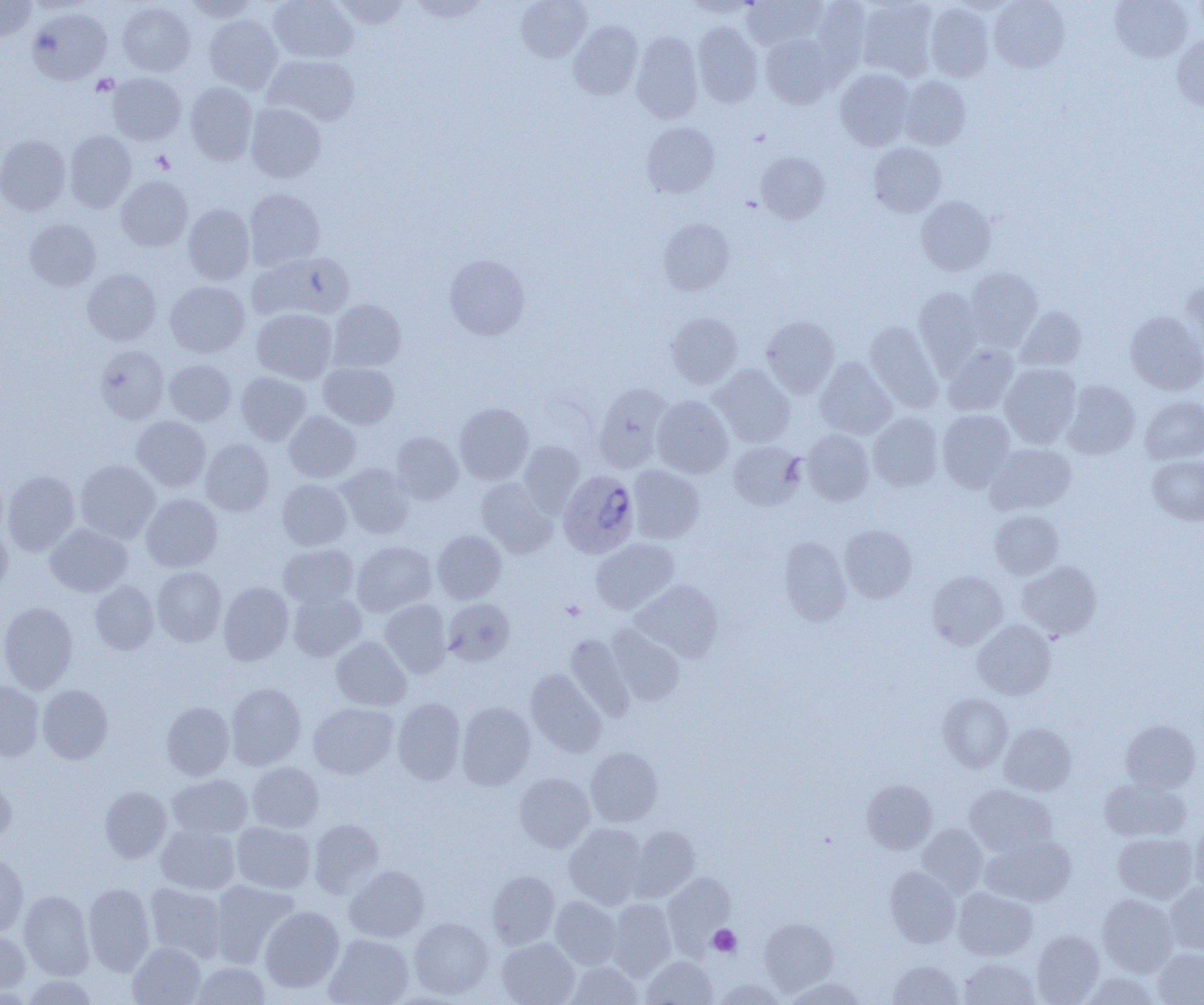
slide_level_diagnosis: Plasmodium ovale
modality: light microscopy
image_size: 1204×1005 pixels
magnification: 1000x
platelet_locations: 'approximate bounding boxes as (x1,y1)-(x2,y2) corner pairs in pixels: (91,74)-(118,96), (151,151)-(175,174), (561,600)-(585,621), (708,925)-(741,957)'
preparation: thin blood film
field_of_view: single
plasmodium_ovale_infected_red_blood_cell_locations: 'approximate bounding boxes as (x1,y1)-(x2,y2) corner pairs in pixels: (559,470)-(639,557)'
uninfected_red_blood_cell_locations: 'approximate bounding boxes as (x1,y1)-(x2,y2) corner pairs in pixels: (0,0)-(36,41), (185,0)-(260,21), (269,0)-(358,63), (331,0)-(411,29), (408,0)-(492,22), (516,0)-(591,62), (683,0)-(757,18), (742,0)-(827,50), (857,0)-(938,80), (989,0)-(1070,72), (1110,0)-(1193,62), (812,1)-(871,77), (117,2)-(195,76), (925,2)-(994,82), (27,8)-(111,84), (204,14)-(282,94), (569,21)-(642,99), (693,22)-(762,108), (631,32)-(703,123), (760,33)-(840,108), (1172,34)-(1204,109), (264,54)-(360,126), (835,68)-(915,150), (107,73)-(186,145), (900,77)-(971,150), (184,82)-(258,165), (245,103)-(326,183), (642,122)-(719,198), (64,130)-(136,213), (0,135)-(70,215), (868,142)-(946,217), (755,152)-(830,223), (116,177)-(192,252), (245,188)-(325,270), (916,196)-(996,276), (183,204)-(254,285), (25,219)-(100,291), (659,219)-(734,295), (247,252)-(354,322), (444,254)-(530,340), (965,268)-(1042,349), (83,269)-(161,345), (1180,280)-(1204,367), (165,281)-(249,357), (913,286)-(984,372), (328,300)-(406,371), (1016,306)-(1086,372), (252,308)-(337,384), (1125,311)-(1204,395), (666,312)-(743,388), (762,316)-(839,396), (865,322)-(942,411), (942,343)-(1019,416), (95,346)-(169,424), (815,357)-(896,439), (165,359)-(236,425), (319,362)-(399,429), (999,363)-(1081,448), (711,364)-(795,447), (236,372)-(311,444), (1063,380)-(1140,459), (593,383)-(671,472), (652,395)-(733,478), (1140,397)-(1204,463), (454,403)-(533,484), (284,410)-(361,482), (936,410)-(1015,492), (868,413)-(943,491), (132,415)-(211,491), (802,429)-(875,506), (391,432)-(463,504), (200,438)-(274,517), (519,441)-(585,515), (728,441)-(805,510), (984,442)-(1076,515), (1147,455)-(1204,525), (75,460)-(160,542), (337,464)-(414,539), (628,465)-(705,544), (2,470)-(79,556), (477,478)-(557,557), (277,479)-(352,550), (141,494)-(222,572), (990,510)-(1063,579), (0,521)-(12,599), (45,524)-(132,596), (839,525)-(917,602), (432,530)-(506,604), (779,537)-(851,625), (591,538)-(678,614), (352,541)-(436,617), (277,544)-(358,609), (1016,561)-(1101,639), (152,566)-(226,646), (927,571)-(1008,649), (90,580)-(159,654), (631,580)-(722,662), (218,581)-(293,665), (288,591)-(365,661), (443,598)-(515,665), (379,599)-(452,677), (0,601)-(77,693), (972,619)-(1055,700), (606,625)-(685,705), (565,634)-(635,721), (331,636)-(411,711), (526,668)-(606,757), (0,681)-(44,762), (225,682)-(306,770), (38,684)-(113,764), (938,693)-(1013,772), (393,698)-(465,784), (161,701)-(234,780), (456,702)-(535,790), (309,703)-(398,779), (1120,719)-(1201,793), (999,722)-(1076,795), (586,747)-(662,826), (247,762)-(324,832), (0,773)-(16,844), (514,773)-(595,852), (166,774)-(252,840), (1099,778)-(1191,842), (862,779)-(937,854), (965,785)-(1057,857), (99,786)-(172,863), (309,818)-(383,898), (1190,818)-(1204,895), (231,821)-(315,894), (564,823)-(646,908), (917,823)-(988,897), (156,824)-(240,895), (629,826)-(700,901), (1113,833)-(1197,903), (982,835)-(1075,906), (0,852)-(29,937), (344,865)-(429,942), (885,866)-(960,947), (487,870)-(560,948), (663,873)-(737,954), (209,880)-(300,968), (1165,882)-(1204,955), (83,883)-(155,975), (145,883)-(227,963), (953,888)-(1037,960), (19,890)-(95,980), (1098,894)-(1177,976), (550,896)-(621,969), (608,899)-(675,980), (260,906)-(344,992), (409,917)-(493,999), (759,918)-(838,995), (0,929)-(31,997), (1032,930)-(1104,1004), (324,934)-(413,1005), (497,937)-(579,1005), (128,941)-(205,1005), (958,946)-(1104,1005), (1153,948)-(1204,1005), (642,956)-(717,1004), (959,958)-(1039,1004), (888,960)-(963,1004), (192,961)-(270,1005), (567,962)-(642,1005), (1082,973)-(1160,1005), (19,975)-(100,1004), (784,977)-(866,1005), (713,979)-(785,1005)'